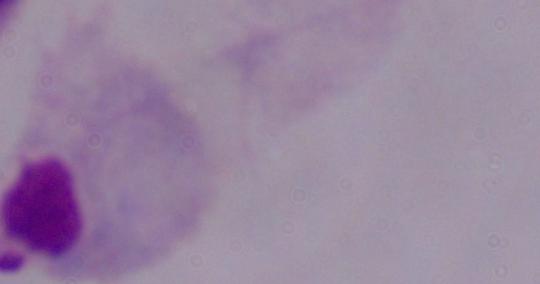

1000x magnification. Photomicrograph. A trichomonad is seen.